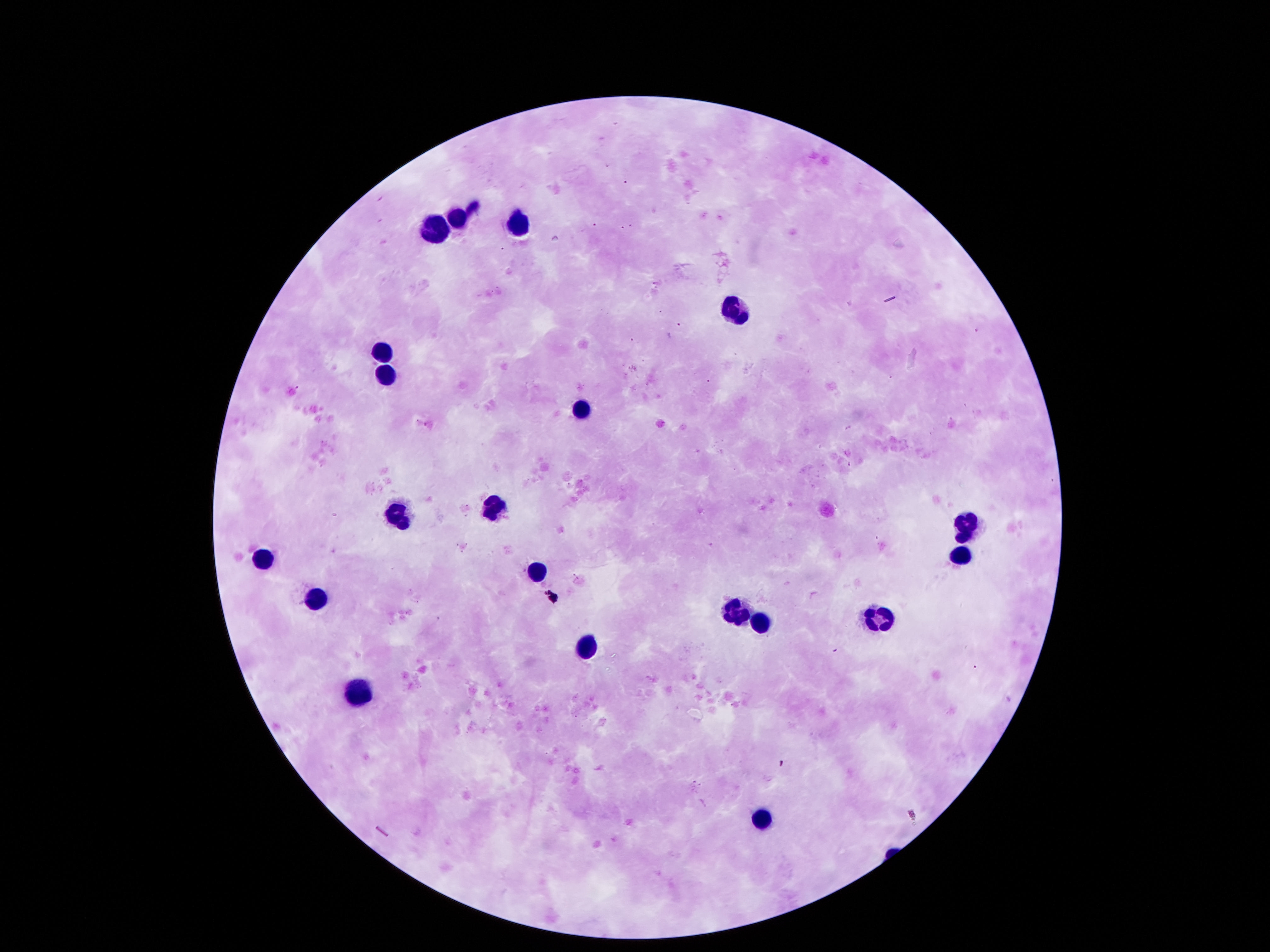
Approximate centers as (x, y) in pixels. Leukocyte locations: (455, 222), (515, 225), (428, 229), (737, 304), (380, 352), (383, 370), (581, 409), (494, 508), (398, 510), (965, 528), (962, 556), (263, 561), (536, 567), (314, 597), (737, 616), (881, 618), (761, 625), (584, 648), (359, 694), (764, 819). 100x magnification. Single field of view. Image is 1270×952 pixels. Giemsa stain. Photographed through the microscope eyepiece with a smartphone camera. Thick blood film. Patient malaria status: not infected.